Locate platelets.
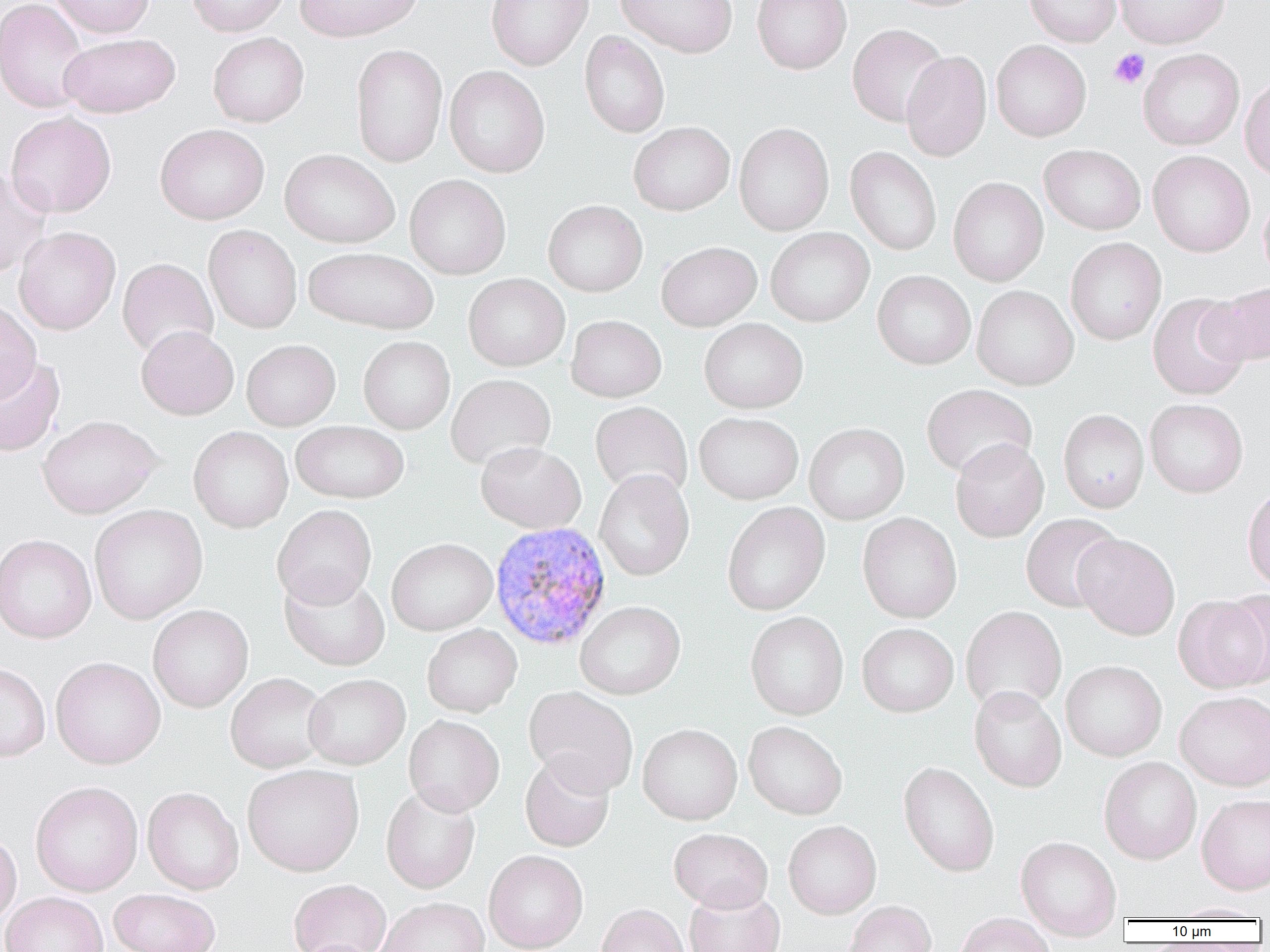

Approximate bounding boxes as (x1,y1)-(x2,y2) corner pairs in pixels.
Platelets: (1109,48)-(1150,89).

Plasmodium vivax-infected red blood cell locations: (490,521)-(612,651). Uninfected red blood cell locations: (0,0)-(91,114), (50,0)-(154,38), (187,0)-(289,37), (294,0)-(424,42), (486,0)-(593,70), (615,0)-(738,58), (752,0)-(851,74), (1024,0)-(1121,46), (1114,0)-(1230,48), (848,24)-(949,126), (579,31)-(670,138), (208,32)-(309,127), (59,33)-(179,117), (991,40)-(1091,141), (350,44)-(448,168), (1138,48)-(1244,150), (900,51)-(991,162), (444,66)-(550,178), (1240,74)-(1270,180), (5,112)-(116,217), (629,122)-(734,215), (734,123)-(834,236), (155,124)-(269,224), (1039,144)-(1145,235), (846,147)-(941,256), (280,149)-(399,248), (1148,151)-(1254,257), (0,168)-(51,279), (405,174)-(511,279), (948,177)-(1048,286), (1258,191)-(1270,287), (543,200)-(647,296), (203,225)-(302,333), (14,227)-(120,335), (766,227)-(874,327), (1066,238)-(1166,345), (656,241)-(761,331), (303,246)-(438,334), (117,258)-(218,359), (872,270)-(975,369), (463,273)-(570,371), (1203,283)-(1270,366), (972,285)-(1079,390), (1147,293)-(1251,400), (0,300)-(41,404), (566,315)-(666,402), (699,318)-(808,413), (136,326)-(238,420), (358,336)-(455,434), (241,339)-(340,431), (0,355)-(65,456), (445,374)-(556,470), (922,384)-(1037,479), (1145,399)-(1248,497), (590,401)-(692,499), (1058,409)-(1149,513), (694,412)-(803,504), (37,415)-(161,518), (291,421)-(409,503), (804,423)-(909,524), (188,426)-(293,533), (950,439)-(1049,542), (476,442)-(586,533), (594,469)-(694,581), (1242,484)-(1270,592), (722,502)-(830,615), (89,505)-(208,624), (272,505)-(377,609), (857,512)-(962,623), (1020,513)-(1122,613), (1073,533)-(1180,640), (0,535)-(96,643), (387,538)-(497,635), (279,571)-(390,671), (1175,595)-(1269,693), (576,601)-(685,699), (148,605)-(253,712), (961,606)-(1066,715), (745,612)-(848,720), (857,623)-(958,717), (422,624)-(522,717), (51,657)-(165,769), (1061,661)-(1166,762), (0,663)-(51,762), (225,673)-(330,773), (304,674)-(410,769), (969,686)-(1066,792), (524,687)-(639,796), (1175,692)-(1270,791), (404,715)-(504,815), (743,721)-(847,820), (637,724)-(742,825), (520,753)-(615,851), (1100,758)-(1201,864), (899,762)-(999,877), (242,764)-(364,876), (30,782)-(142,896), (381,784)-(480,894), (142,787)-(244,894), (1197,794)-(1270,895), (783,821)-(881,919), (669,828)-(773,913), (0,831)-(21,927), (1016,837)-(1122,941), (484,851)-(588,952), (288,880)-(391,952), (109,888)-(220,952), (684,888)-(784,952), (1,892)-(108,952), (376,898)-(489,952), (844,902)-(937,952), (1170,902)-(1265,921), (595,904)-(690,952), (955,913)-(1055,952), (296,939)-(380,952). Slide-level diagnosis: Plasmodium vivax. Single field of view. Thin blood smear. Captured at 1000x magnification. Image is 1270×952 pixels. Optical microscopy.